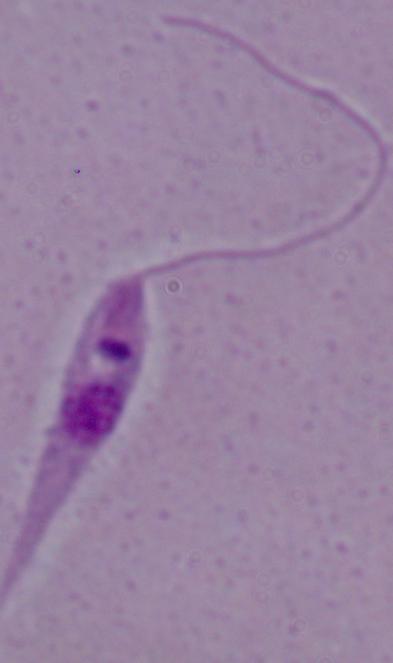

Summary:
  - Identification: Leishmania
  - Magnification: 1000x
  - Modality: micrograph